Classify this cell by malaria status.
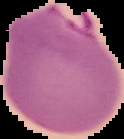

Parasitized.

image size = 124×139 pixels
preparation = thin blood film
image type = segmented cell region with the area outside set to black